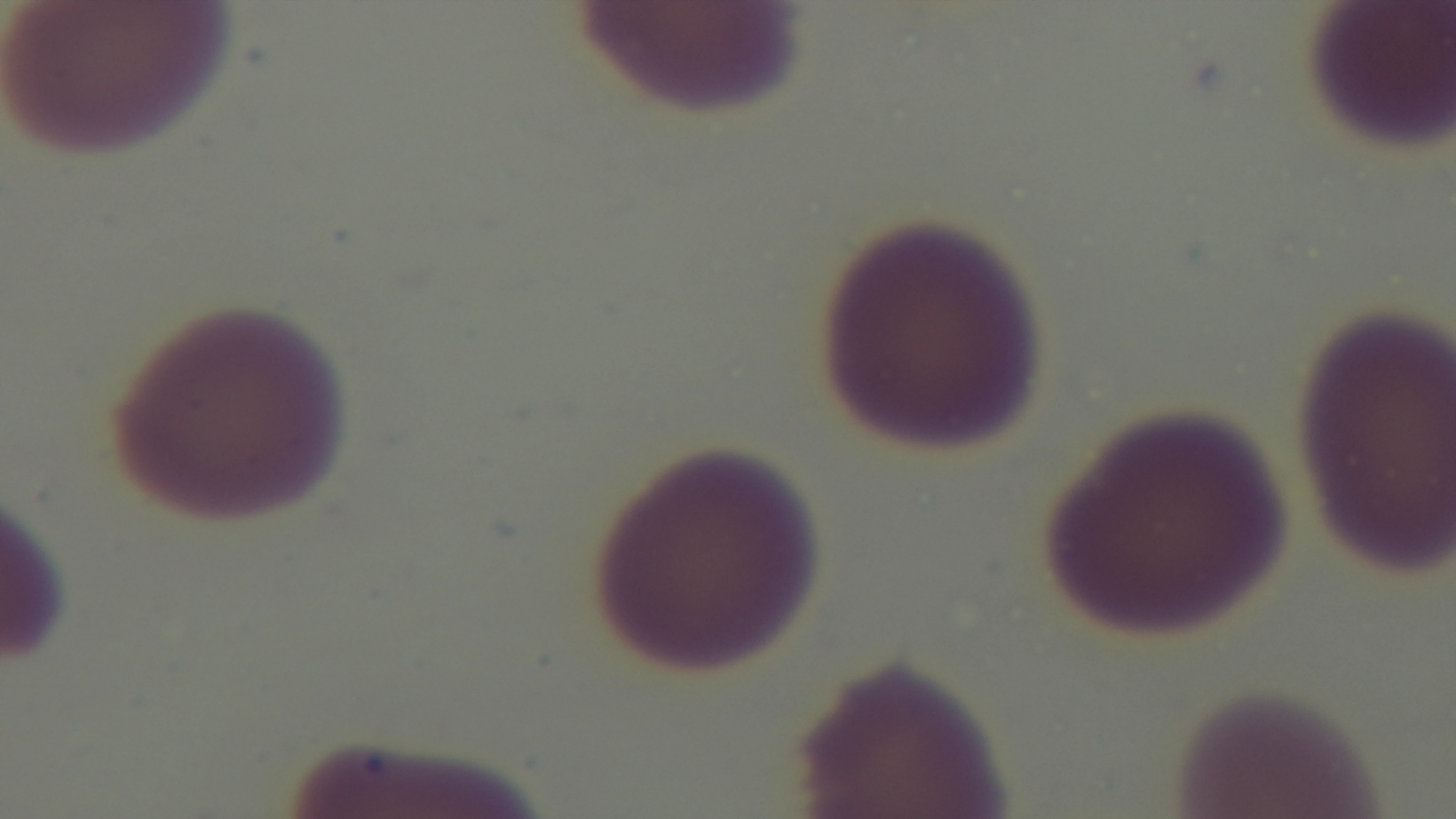 Giemsa-stained. Malaria status: uninfected. Single field of view. Oil-immersion objective, 100x. Preparation: thin smear. Light microscopy. Mounted 4K digital camera.